Assess this cell for malaria.
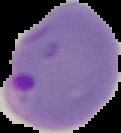

It is parasitized.

From a thin blood smear. Segmented cell region on a black background. Image is 121×133 pixels.